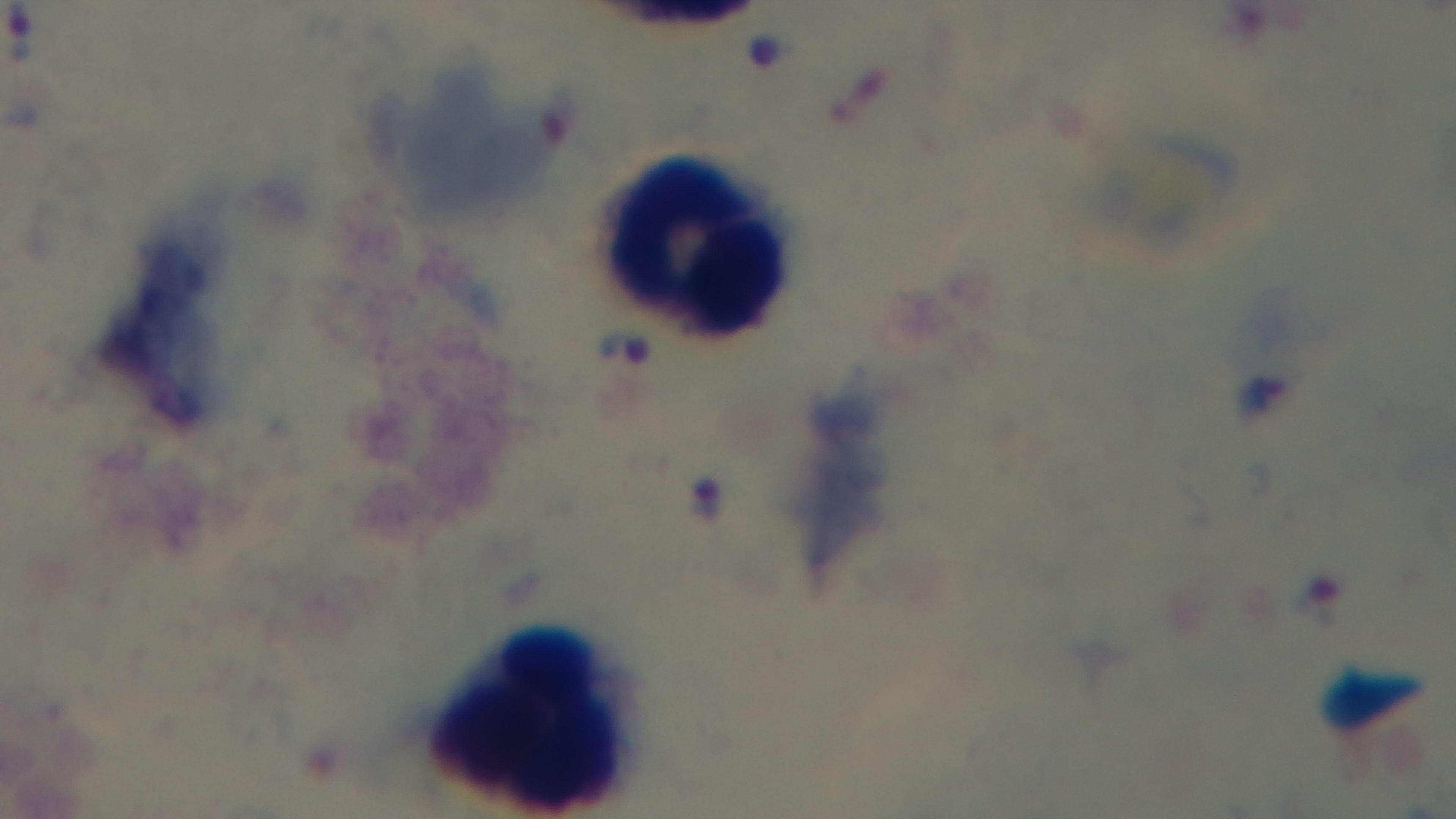
capture = mounted 4K digital camera
preparation = thick
field of view = one from the slide
objective = 100x oil immersion
stain = Giemsa
modality = light microscopy
malaria status = infected